Identify the cell.
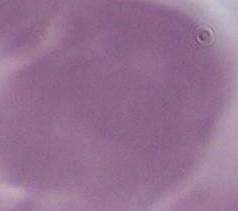

This is an erythrocyte.

Summary:
  - Magnification: 1000x
  - Modality: photomicrograph